Describe the morphology of the red blood cells.
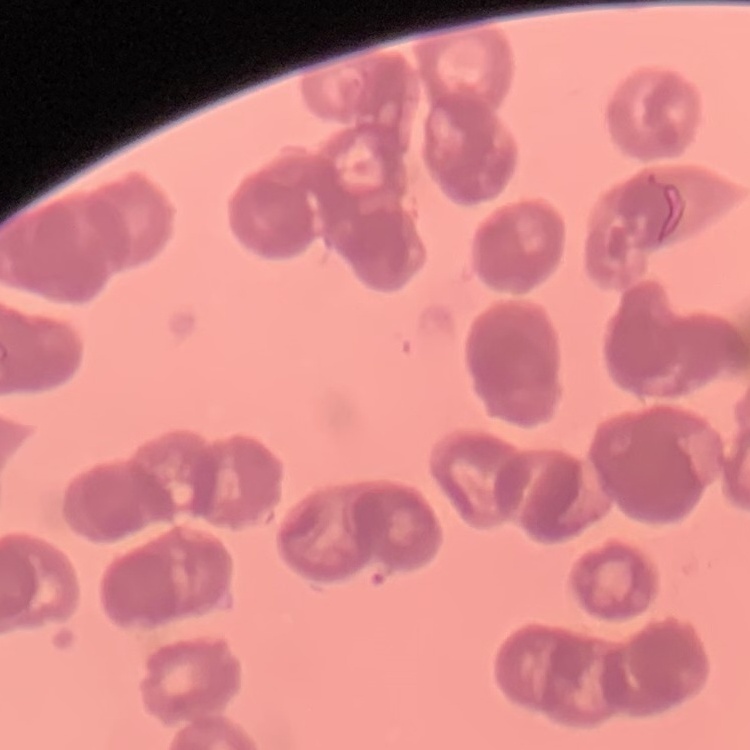

Rouleaux formation.

stain = Field's or Giemsa
preparation = thin blood film
image type = square crop of a larger photomicrograph